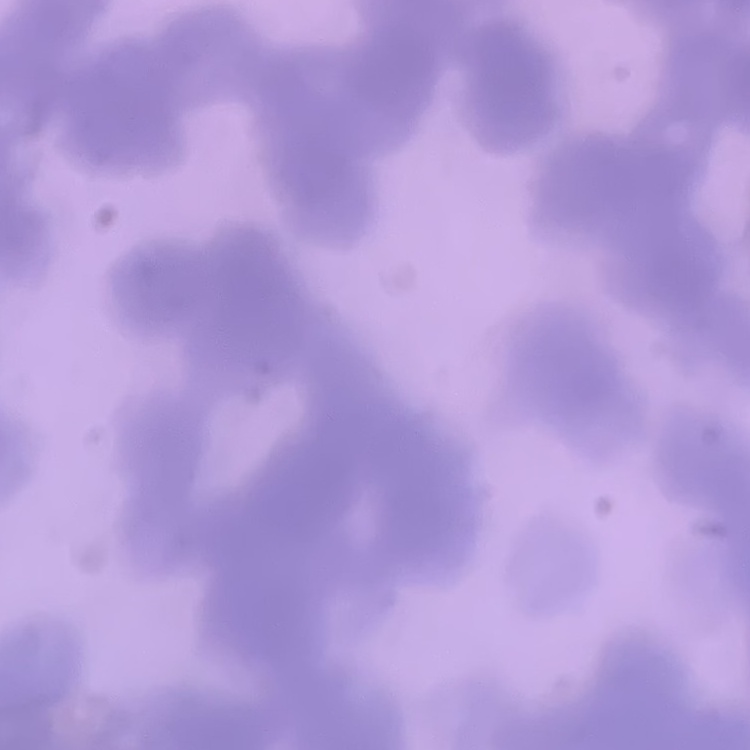

Summary:
  - Red blood cell morphology: rouleaux formation
  - Stain: Field's or Giemsa
  - Preparation: thin blood smear
  - Image type: one tile cut from a larger photomicrograph